Locate every Plasmodium ovale-infected red blood cell.
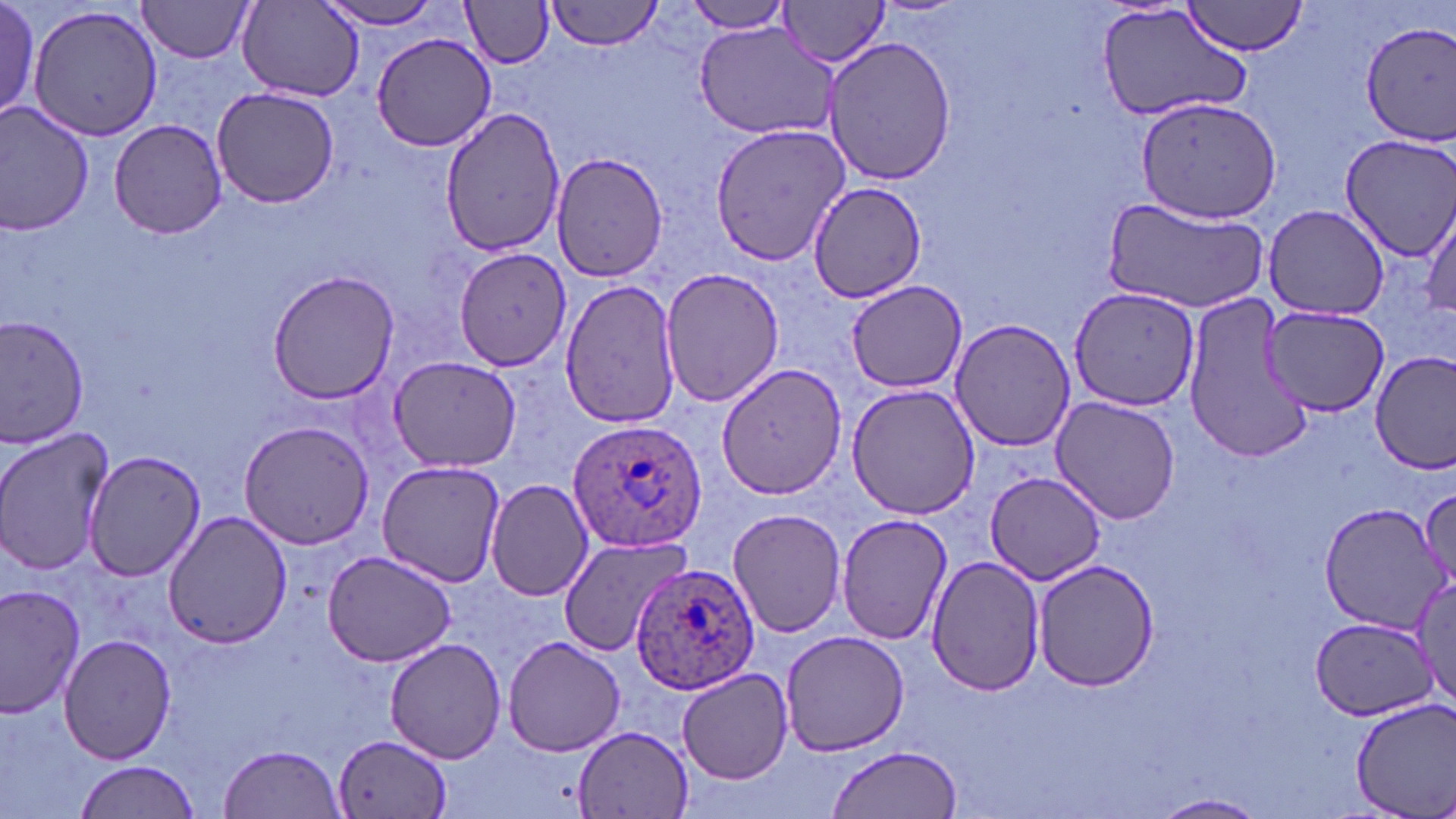
Approximate bounding boxes as (x1, y1, x2, y2) in pixels.
Plasmodium ovale-infected red blood cells: (569, 419, 705, 552), (633, 563, 762, 698).

Uninfected red blood cell locations: (0, 0, 41, 118), (137, 0, 257, 62), (543, 0, 663, 52), (774, 0, 893, 68), (316, 2, 448, 30), (462, 2, 554, 68), (680, 2, 795, 35), (1181, 2, 1311, 59), (239, 3, 361, 98), (1095, 3, 1253, 124), (27, 4, 167, 143), (692, 18, 844, 139), (1360, 21, 1456, 144), (369, 32, 498, 153), (820, 35, 958, 188), (211, 86, 342, 209), (1134, 94, 1284, 226), (0, 103, 95, 235), (439, 107, 567, 256), (108, 118, 230, 239), (711, 120, 850, 266), (1339, 134, 1456, 259), (550, 150, 669, 281), (809, 180, 928, 303), (1103, 197, 1269, 311), (1421, 203, 1455, 327), (1264, 205, 1390, 319), (457, 248, 575, 372), (659, 266, 784, 410), (268, 269, 399, 404), (559, 278, 682, 429), (843, 279, 968, 392), (1067, 285, 1200, 410), (1180, 292, 1315, 466), (1260, 302, 1390, 416), (0, 315, 92, 446), (948, 319, 1075, 450), (1370, 350, 1456, 477), (388, 357, 521, 471), (716, 362, 847, 500), (847, 384, 981, 520), (1050, 396, 1180, 523), (239, 420, 374, 549), (0, 426, 115, 576), (81, 450, 208, 582), (376, 460, 508, 588), (988, 473, 1106, 586), (487, 479, 595, 601), (1416, 484, 1455, 600), (1318, 503, 1443, 631), (727, 506, 846, 638), (163, 511, 292, 648), (837, 514, 955, 645), (557, 535, 691, 658), (321, 550, 460, 668), (925, 554, 1048, 697), (1031, 560, 1159, 689), (1412, 575, 1456, 703), (0, 584, 87, 717), (1310, 617, 1431, 719), (779, 629, 912, 756), (58, 633, 178, 763), (502, 635, 627, 756), (384, 636, 507, 764), (678, 669, 794, 783), (1347, 696, 1456, 819), (572, 726, 694, 817), (334, 732, 451, 818), (218, 744, 345, 818), (827, 745, 963, 818), (74, 759, 199, 818), (1152, 792, 1270, 817). Slide-level diagnosis: Plasmodium ovale. 1000x magnification. Image is 1456×819 pixels. May-Grünwald-Giemsa-stained preparation. Single field of view. Thin blood smear. Optical microscopy.